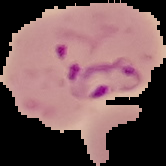
Summary:
  - Image type: segmented cell region on a black background
  - Preparation: thin blood film
  - Image size: 166×166 pixels
  - Result: malaria parasites identified